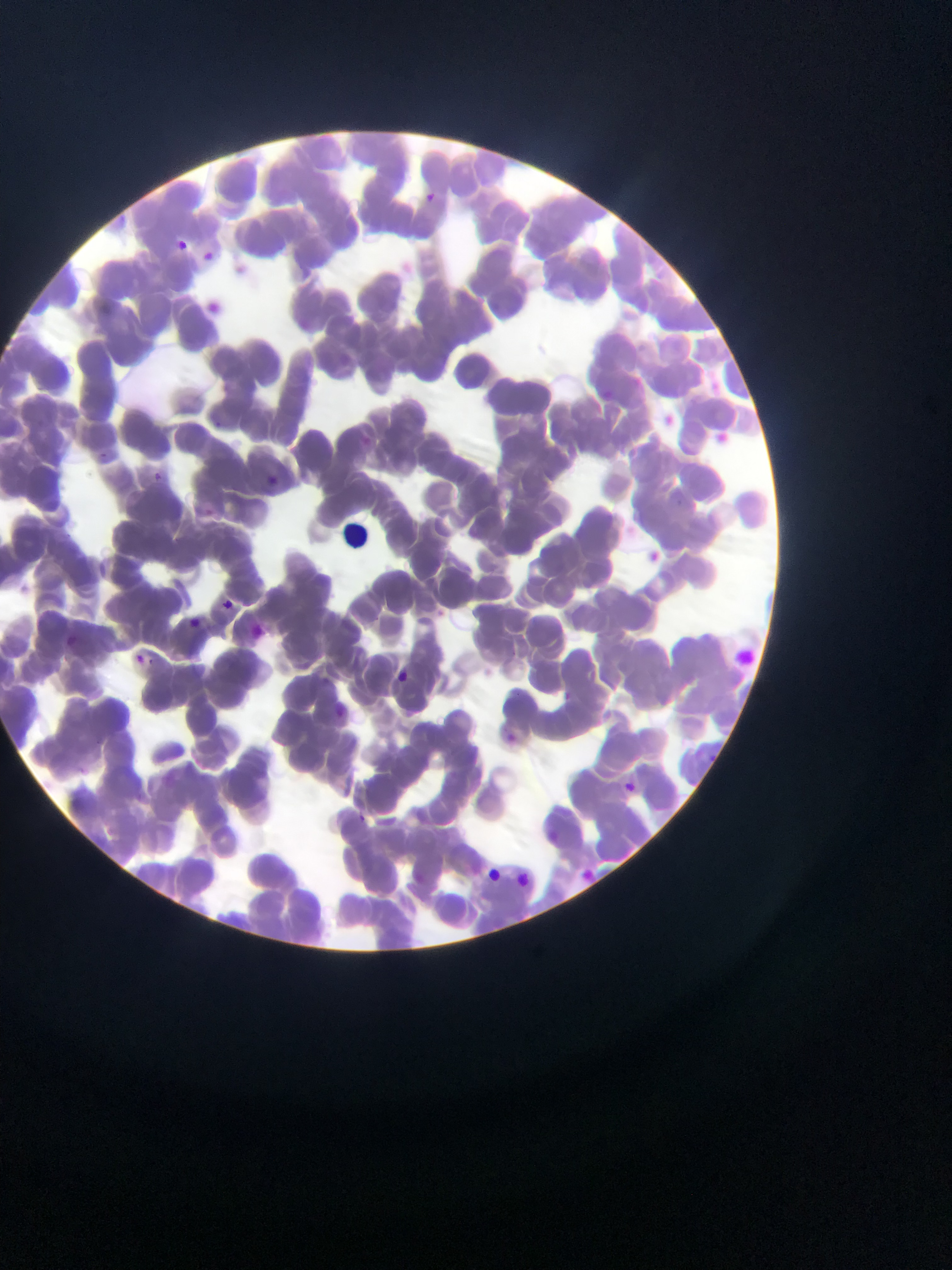 Approximate bounding boxes as [left, top, right, bottom] in pixels. Leukocyte locations: [338, 514, 381, 558]. Plasmodium parasite locations: [421, 191, 441, 208], [169, 235, 191, 258], [198, 246, 219, 266], [233, 261, 253, 280], [151, 471, 163, 483], [263, 472, 282, 489], [641, 550, 664, 570], [218, 596, 236, 613], [185, 615, 203, 631], [130, 649, 167, 660], [390, 668, 414, 690], [499, 732, 519, 752], [620, 778, 639, 796], [353, 810, 373, 826], [480, 864, 504, 887], [576, 866, 601, 889], [511, 870, 532, 891]. Photographed through a microscope with a mobile-phone camera. Thin blood film. One field of view. Sample from Ghana. Image is 952×1270 pixels.